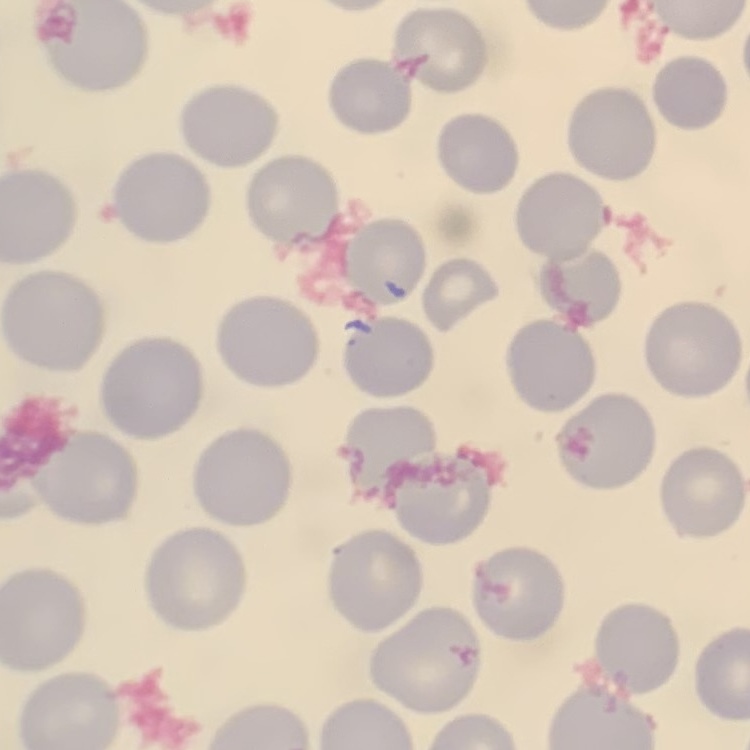

The erythrocytes show no rouleaux formation. Thin blood smear. Square crop of a larger photomicrograph. Field's or Giemsa stain.